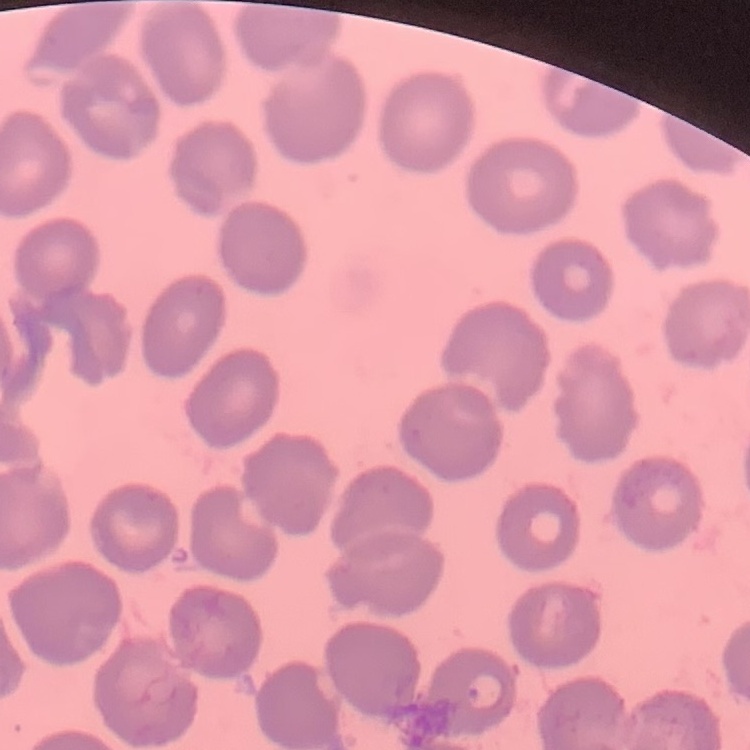
Summary:
  - Red blood cell morphology: no rouleaux formation
  - Preparation: thin peripheral smear
  - Image type: square crop of a larger photomicrograph
  - Stain: Field's or Giemsa